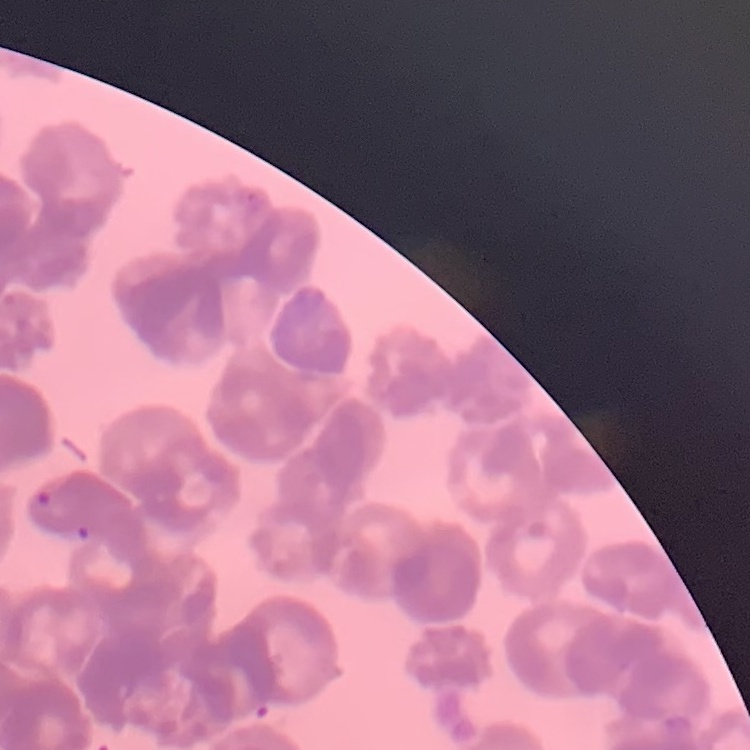
Summary:
  - Erythrocyte morphology: rouleaux formation
  - Image type: one tile cut from a larger photomicrograph
  - Preparation: thin peripheral smear
  - Stain: Field's or Giemsa